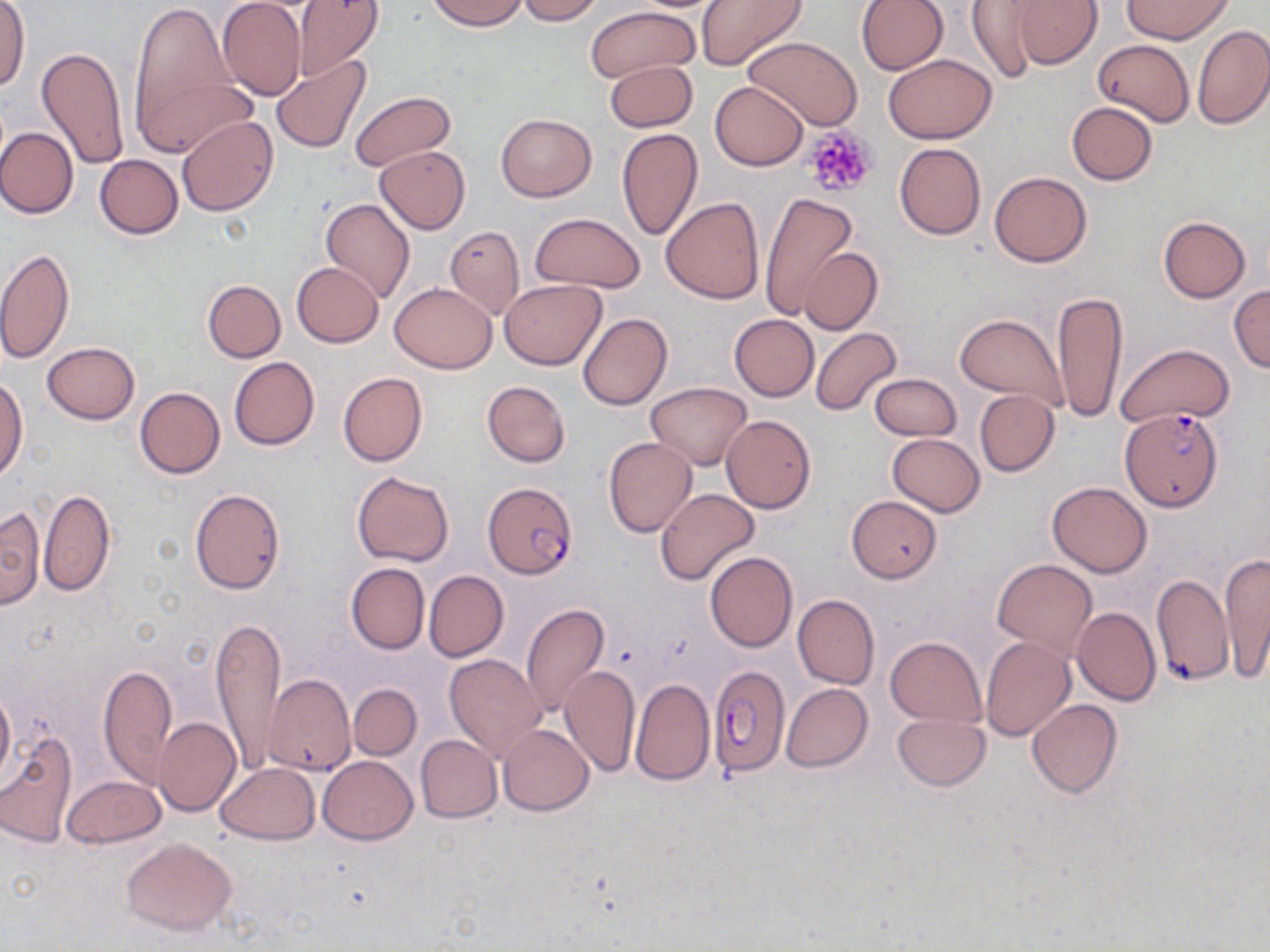 Approximate bounding boxes as (x1, y1, x2, y2) in pixels. Plasmodium falciparum-infected red blood cell locations: (1121, 407, 1223, 512), (484, 482, 577, 579), (709, 668, 790, 776). Uninfected red blood cell locations: (128, 0, 243, 151), (427, 0, 529, 31), (516, 0, 604, 24), (696, 0, 809, 70), (855, 0, 948, 75), (1009, 0, 1101, 69), (1124, 0, 1232, 43), (216, 1, 305, 101), (288, 1, 383, 80), (963, 2, 1047, 83), (0, 3, 29, 93), (586, 5, 701, 83), (1192, 24, 1270, 128), (741, 35, 864, 133), (1093, 39, 1193, 126), (36, 44, 130, 170), (883, 54, 996, 143), (272, 55, 373, 156), (605, 59, 697, 131), (141, 71, 256, 159), (709, 80, 808, 169), (348, 89, 457, 171), (1068, 102, 1157, 184), (495, 113, 596, 201), (177, 115, 278, 217), (0, 126, 78, 219), (616, 129, 702, 240), (894, 143, 986, 239), (374, 145, 471, 233), (95, 154, 183, 238), (989, 171, 1091, 267), (760, 192, 858, 321), (321, 198, 415, 304), (661, 198, 765, 303), (530, 213, 646, 292), (1158, 216, 1250, 302), (444, 225, 525, 320), (799, 246, 882, 334), (0, 248, 73, 365), (291, 263, 383, 348), (499, 279, 606, 369), (202, 280, 285, 362), (389, 283, 498, 373), (1229, 284, 1270, 371), (1052, 289, 1128, 421), (953, 312, 1066, 411), (577, 313, 673, 410), (729, 314, 818, 401), (810, 326, 902, 417), (42, 342, 140, 424), (1113, 343, 1234, 428), (229, 357, 319, 450), (339, 372, 427, 467), (869, 373, 962, 441), (0, 377, 27, 479), (482, 381, 571, 468), (646, 381, 752, 469), (134, 387, 224, 479), (974, 390, 1060, 477), (720, 415, 815, 512), (887, 433, 985, 517), (603, 438, 697, 537), (352, 471, 453, 566), (1047, 482, 1153, 577), (655, 487, 760, 585), (190, 488, 285, 594), (40, 489, 115, 595), (846, 496, 942, 582), (1, 506, 45, 611), (705, 551, 797, 652), (1219, 553, 1270, 681), (992, 558, 1096, 660), (346, 562, 430, 654), (423, 570, 508, 661), (1153, 572, 1233, 688), (792, 594, 879, 689), (521, 604, 610, 718), (1072, 607, 1160, 705), (212, 616, 286, 771), (886, 637, 986, 726), (980, 637, 1075, 741), (445, 654, 547, 761), (98, 664, 177, 787), (560, 664, 640, 777), (264, 674, 356, 777), (630, 679, 714, 786), (348, 683, 422, 761), (782, 684, 872, 772), (0, 689, 15, 784), (1028, 700, 1123, 798), (892, 714, 989, 790), (153, 717, 240, 816), (498, 723, 593, 816), (0, 731, 78, 848), (416, 735, 501, 822), (318, 755, 419, 844), (216, 762, 319, 843), (62, 775, 165, 848), (122, 837, 236, 934). Platelet locations: (801, 125, 880, 198). Slide-level diagnosis: Plasmodium falciparum. Light microscopy. One field of a larger specimen. Captured at 1000x magnification. Thin blood smear. May-Grünwald-Giemsa-stained preparation. Image is 1270×952 pixels.